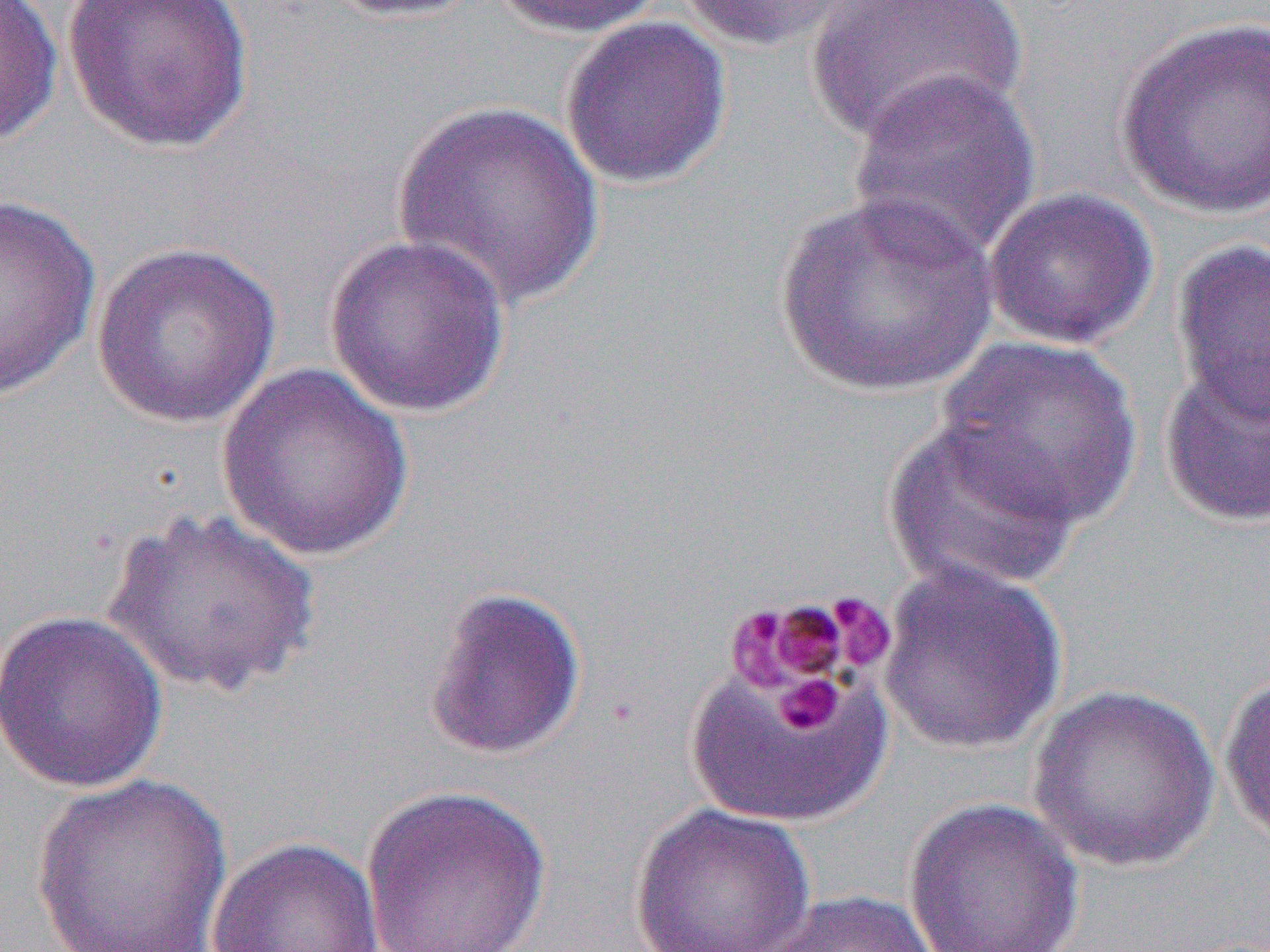

Summary:
  - Coordinate format: approximate bounding boxes as [x1, y1, x2, y2] in pixels
  - Platelet locations: [824, 592, 896, 672], [726, 595, 868, 700], [688, 671, 888, 823], [775, 674, 843, 735]
  - Uninfected red blood cell locations: [0, 0, 64, 148], [61, 0, 255, 155], [321, 0, 486, 22], [488, 0, 665, 39], [676, 0, 863, 53], [805, 0, 1026, 146], [559, 16, 732, 189], [1114, 16, 1269, 221], [846, 67, 1042, 266], [392, 99, 605, 311], [983, 186, 1158, 350], [773, 191, 997, 398], [0, 193, 102, 402], [322, 233, 512, 419], [1171, 238, 1270, 423], [90, 240, 282, 429], [934, 335, 1146, 531], [1159, 358, 1270, 528], [215, 363, 415, 561], [882, 418, 1081, 596], [100, 505, 324, 702], [878, 560, 1067, 756], [421, 585, 587, 761], [0, 609, 168, 793], [684, 669, 891, 827], [1219, 671, 1270, 850], [1026, 683, 1221, 872], [32, 773, 231, 950], [357, 783, 555, 952], [902, 796, 1086, 952], [630, 802, 816, 951], [205, 836, 384, 952], [755, 890, 946, 952]
  - Slide-level diagnosis: Plasmodium malariae
  - Magnification: 1000x
  - Preparation: thin blood smear
  - Modality: light microscopy
  - Image size: 1270×952 pixels
  - Field of view: one of a larger specimen